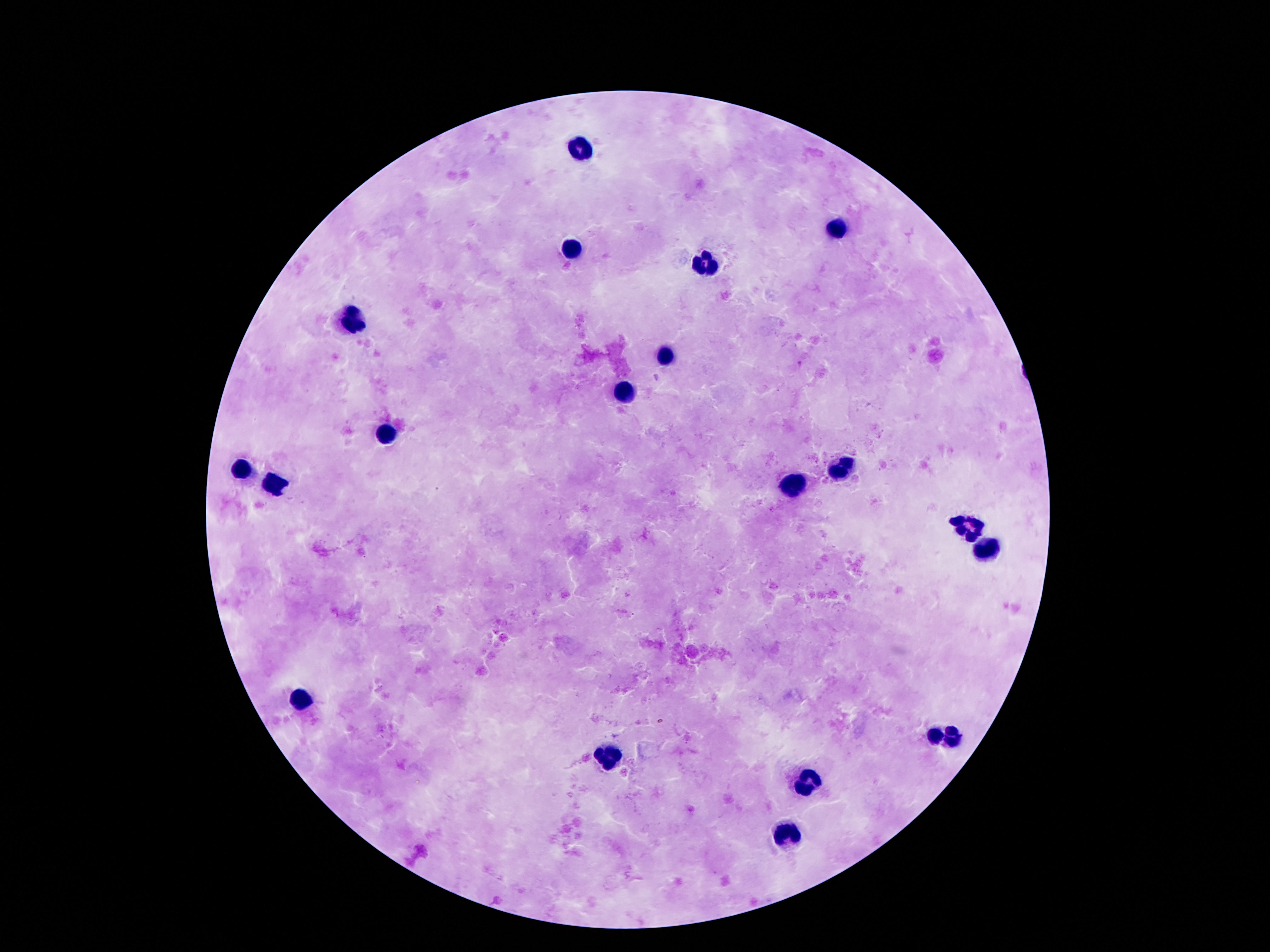

Approximate centers as (x, y) in pixels.
Summary:
  - Leukocyte locations: (581, 150), (840, 230), (574, 250), (706, 264), (349, 317), (665, 357), (627, 395), (385, 433), (840, 470), (241, 472), (792, 486), (276, 487), (969, 526), (984, 549), (300, 700), (945, 735), (603, 755), (800, 783), (788, 834)
  - Capture: smartphone camera through the microscope eyepiece
  - Image size: 1270×952 pixels
  - Patient malaria status: uninfected
  - Stain: Giemsa
  - Magnification: 100x
  - Field of view: single
  - Preparation: thick blood smear